Give the extent of all Babesia divergens-infected red blood cells.
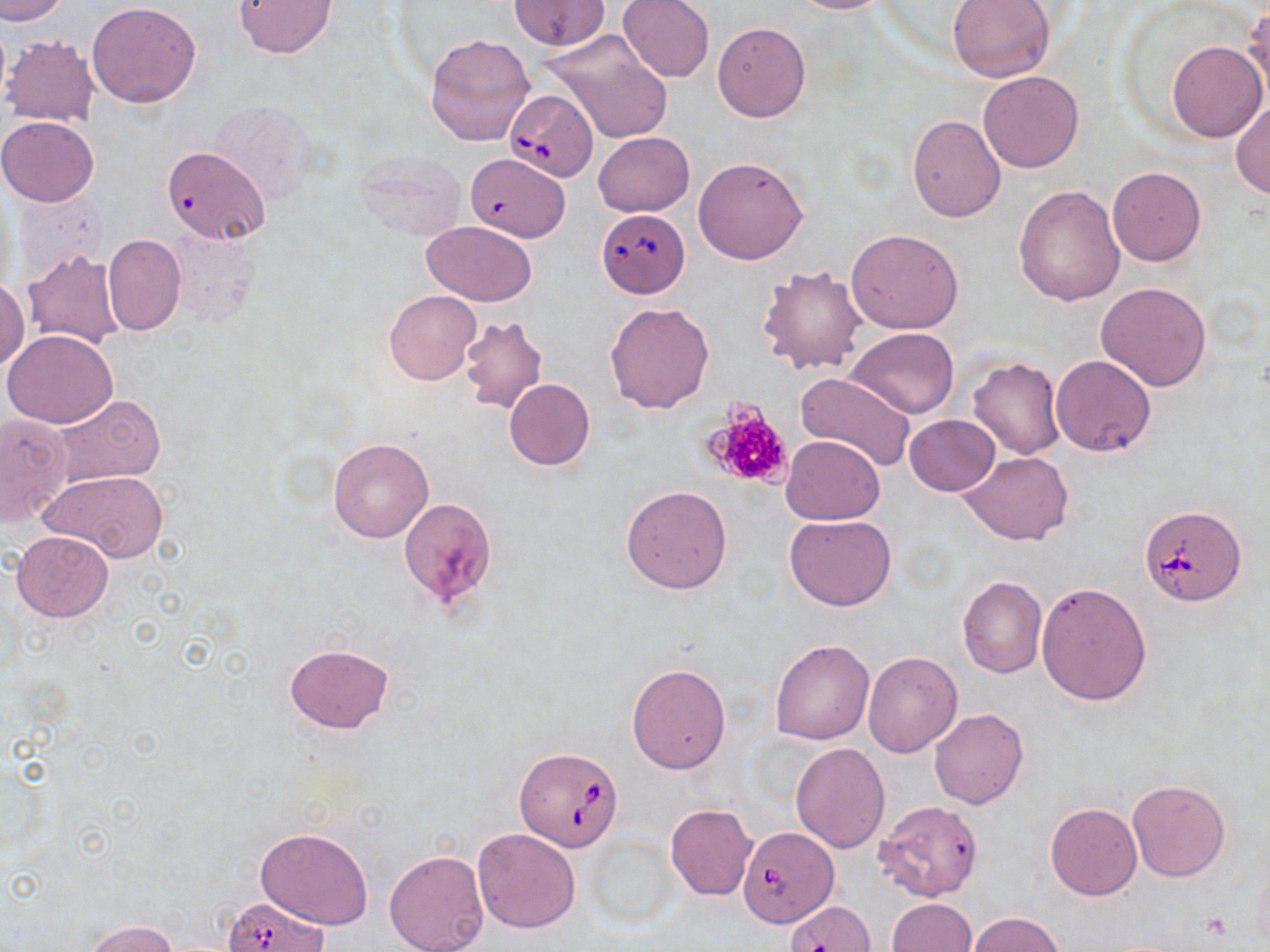

Approximate bounding boxes as [x1, y1, x2, y2] in pixels.
Babesia divergens-infected red blood cells: [504, 90, 599, 182], [465, 153, 576, 248], [595, 209, 690, 299], [1140, 505, 1246, 605], [514, 746, 624, 851], [738, 827, 836, 926], [222, 896, 330, 951].

Platelet locations: [701, 398, 798, 490], [1202, 912, 1234, 941]. Uninfected red blood cell locations: [1, 0, 70, 24], [617, 0, 714, 83], [781, 0, 891, 14], [947, 0, 1058, 83], [87, 1, 202, 108], [232, 1, 335, 57], [508, 1, 612, 52], [1244, 6, 1270, 103], [712, 22, 810, 122], [540, 29, 675, 144], [425, 32, 535, 148], [2, 35, 100, 127], [1167, 41, 1267, 142], [979, 72, 1083, 172], [213, 101, 319, 205], [1232, 101, 1270, 199], [906, 113, 1005, 222], [0, 115, 100, 206], [592, 132, 694, 217], [161, 145, 270, 244], [353, 150, 466, 243], [693, 155, 809, 265], [1107, 167, 1205, 266], [1013, 185, 1126, 306], [14, 192, 102, 283], [422, 220, 538, 307], [167, 228, 258, 326], [847, 229, 963, 333], [103, 234, 186, 335], [20, 247, 125, 351], [757, 265, 868, 374], [0, 280, 29, 370], [1095, 282, 1211, 392], [383, 289, 481, 386], [604, 301, 716, 415], [460, 316, 547, 414], [847, 328, 958, 419], [2, 329, 117, 428], [1051, 354, 1156, 456], [967, 359, 1066, 460], [794, 372, 917, 475], [503, 379, 596, 471], [48, 395, 166, 489], [0, 413, 71, 526], [904, 414, 1000, 497], [780, 434, 886, 525], [327, 438, 434, 542], [960, 452, 1072, 545], [38, 469, 170, 560], [621, 485, 733, 594], [398, 497, 497, 612], [786, 514, 895, 611], [11, 529, 114, 622], [957, 576, 1048, 679], [1036, 581, 1151, 705], [769, 639, 874, 745], [283, 643, 393, 734], [862, 650, 964, 757], [626, 663, 731, 775], [929, 707, 1028, 809], [789, 742, 891, 852], [1127, 777, 1231, 882], [874, 800, 984, 902], [1045, 802, 1142, 900], [664, 804, 758, 900], [256, 826, 375, 929], [472, 827, 582, 932], [384, 849, 490, 952], [886, 898, 976, 952], [966, 911, 1065, 951], [83, 919, 180, 952]. Slide-level diagnosis: Babesia divergens. Image is 1270×952 pixels. Single field of view. Captured at 1000x magnification. Thin blood smear. Optical microscopy. May-Grünwald-Giemsa-stained preparation.